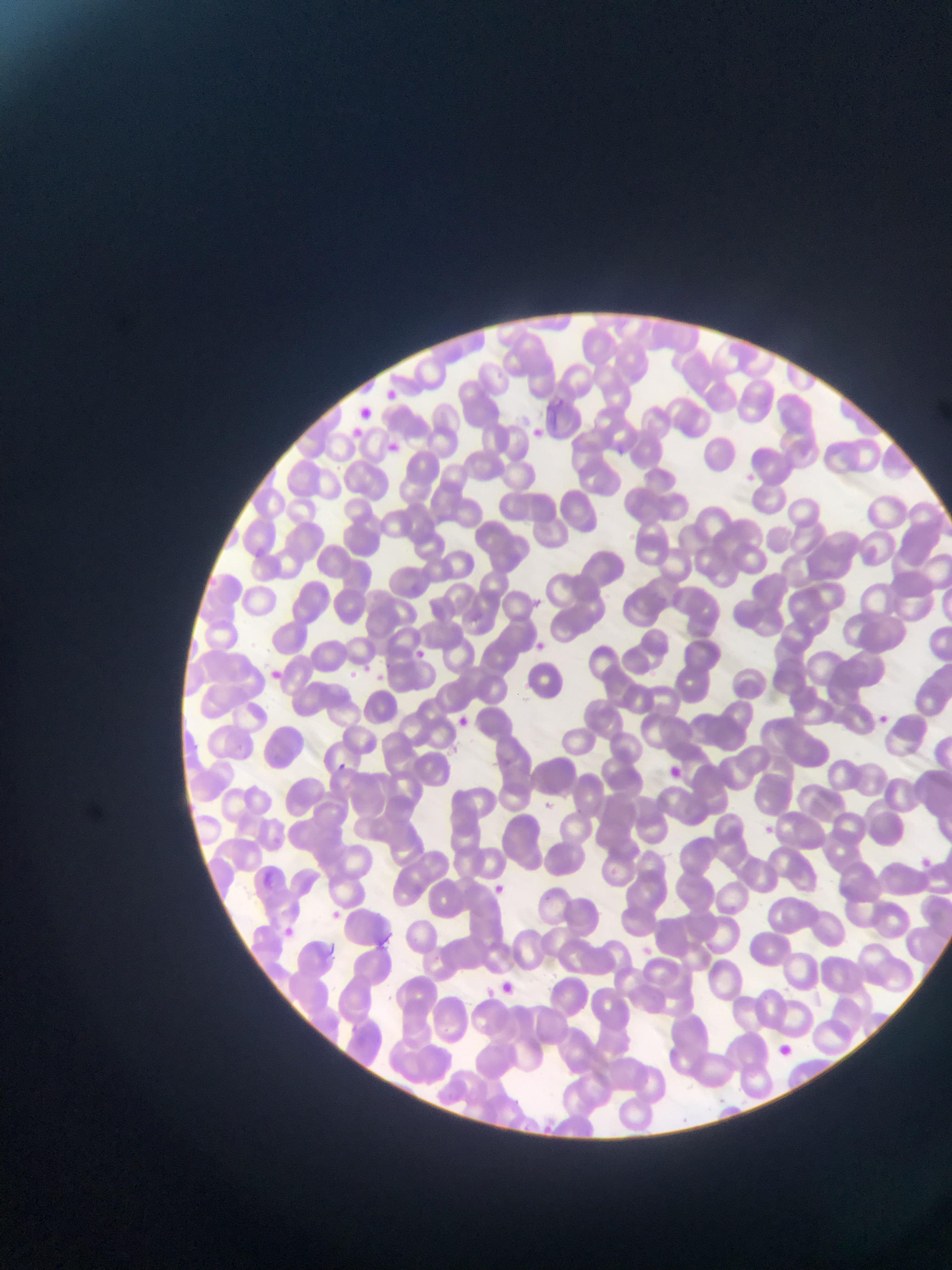
Approximate bounding boxes as (left, top, right, bottom) in pixels.
Summary:
  - Plasmodium parasite locations: (379, 384, 403, 405), (551, 395, 570, 412), (527, 424, 548, 443), (379, 440, 404, 461), (529, 640, 548, 655), (411, 647, 428, 663), (261, 664, 284, 684), (345, 668, 359, 682), (872, 711, 893, 729), (451, 714, 472, 731), (332, 760, 348, 776), (664, 763, 685, 782), (538, 797, 556, 814), (916, 856, 932, 870), (488, 880, 508, 900), (330, 909, 341, 918), (278, 923, 299, 942), (373, 932, 395, 953), (327, 941, 335, 959), (481, 978, 507, 1002), (496, 979, 518, 999), (773, 1041, 793, 1059)
  - Image size: 952×1270 pixels
  - Country: Ghana
  - Field of view: single
  - Capture: mobile-phone photograph through a microscope
  - Preparation: thin blood smear